Classify this cell by malaria status.
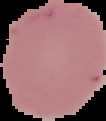
It is uninfected.

image size = 106×121 pixels
image type = segmented cell region on a black background
preparation = thin blood film